Classify this cell by malaria status.
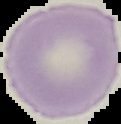

Uninfected.

Image is 121×124 pixels. Segmented cell region on a black background. From a thin blood smear.